Report the malaria status of this cell.
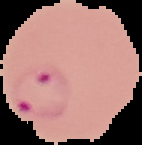

Parasitized.

image_type: cell region segmented out of the field of view; surrounding area masked to black
preparation: thin blood film
image_size: 142×145 pixels